Assess the morphology of the red blood cells.
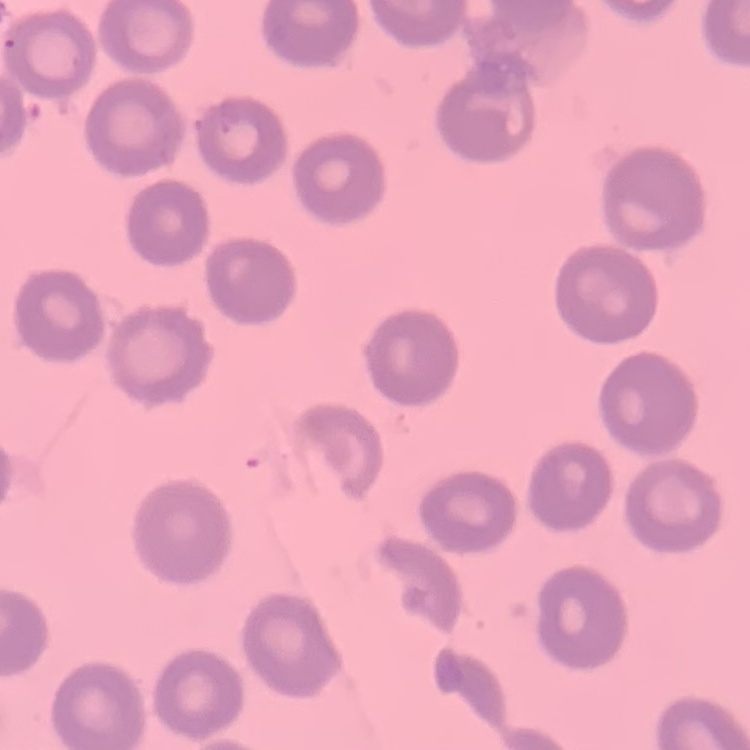
They show no rouleaux formation.

Square crop of a larger photomicrograph. Stained with either Field's or Giemsa. Thin peripheral smear.